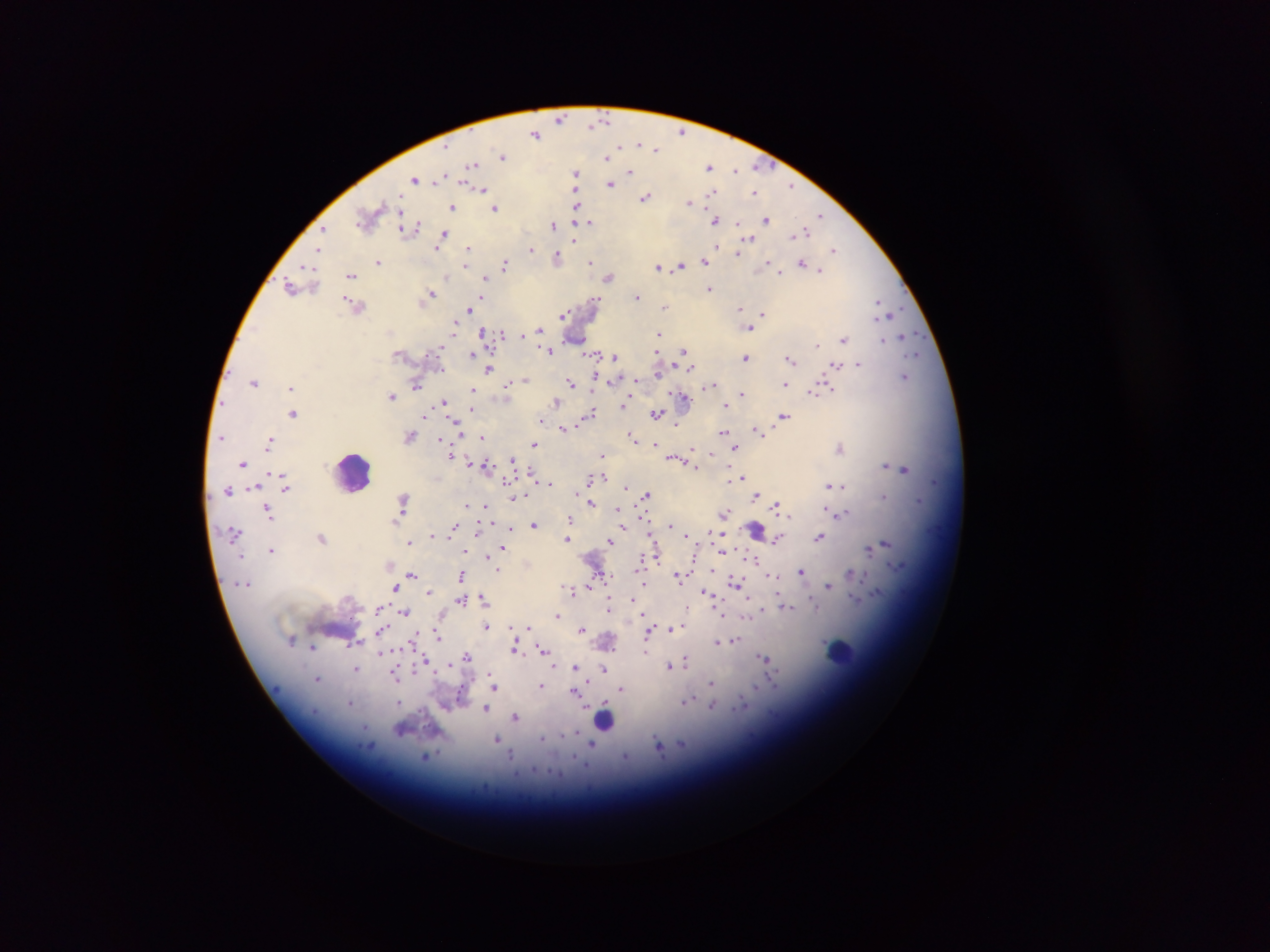

{
  "leukocyte_locations": "approximate centers as {x, y} in pixels: {353, 472}, {841, 651}, {605, 716}",
  "image_size": "1270×952 pixels",
  "field_of_view": "single",
  "country": "Ghana",
  "capture": "mobile-phone photograph through a microscope",
  "preparation": "thick blood smear",
  "plasmodium_parasite_locations": "approximate centers as {x, y} in pixels: {560, 118}, {602, 120}, {595, 122}, {682, 132}, {536, 133}, {638, 144}, {658, 147}, {503, 156}, {609, 156}, {473, 164}, {758, 166}, {710, 167}, {735, 170}, {576, 172}, {630, 172}, {441, 177}, {415, 178}, {612, 184}, {790, 188}, {482, 189}, {714, 192}, {755, 192}, {646, 196}, {576, 202}, {689, 203}, {453, 207}, {495, 208}, {369, 216}, {820, 216}, {767, 218}, {716, 219}, {589, 222}, {554, 225}, {324, 228}, {409, 228}, {801, 232}, {445, 234}, {575, 239}, {749, 239}, {441, 243}, {440, 248}, {319, 250}, {468, 250}, {530, 250}, {833, 250}, {738, 253}, {557, 257}, {705, 261}, {379, 262}, {591, 262}, {504, 264}, {768, 264}, {804, 264}, {466, 266}, {308, 267}, {659, 267}, {680, 267}, {821, 269}, {780, 272}, {350, 274}, {446, 275}, {610, 277}, {486, 279}, {291, 287}, {709, 288}, {430, 294}, {637, 295}, {596, 299}, {480, 302}, {472, 303}, {879, 303}, {354, 304}, {664, 307}, {739, 308}, {883, 308}, {469, 310}, {890, 312}, {763, 313}, {563, 315}, {454, 327}, {749, 328}, {539, 329}, {483, 332}, {504, 332}, {659, 333}, {905, 337}, {844, 339}, {884, 339}, {817, 345}, {439, 347}, {550, 349}, {684, 351}, {472, 353}, {657, 353}, {917, 353}, {597, 354}, {615, 357}, {746, 357}, {791, 359}, {858, 363}, {836, 364}, {490, 368}, {691, 368}, {905, 376}, {597, 377}, {637, 379}, {525, 380}, {254, 382}, {571, 382}, {611, 382}, {416, 384}, {710, 384}, {786, 384}, {508, 385}, {292, 387}, {824, 387}, {473, 390}, {817, 390}, {743, 393}, {393, 396}, {684, 397}, {443, 402}, {557, 402}, {624, 406}, {726, 406}, {472, 410}, {294, 412}, {591, 413}, {657, 413}, {426, 414}, {783, 416}, {541, 419}, {678, 423}, {457, 426}, {564, 427}, {757, 429}, {724, 431}, {411, 435}, {222, 437}, {482, 437}, {634, 437}, {442, 438}, {271, 441}, {535, 443}, {656, 443}, {736, 447}, {841, 447}, {693, 450}, {452, 455}, {603, 455}, {512, 458}, {675, 458}, {468, 462}, {244, 463}, {690, 463}, {474, 464}, {885, 465}, {488, 468}, {904, 469}, {531, 471}, {272, 472}, {283, 473}, {730, 477}, {741, 477}, {591, 480}, {507, 481}, {550, 483}, {624, 486}, {829, 486}, {843, 486}, {286, 487}, {256, 488}, {228, 490}, {524, 493}, {646, 495}, {757, 495}, {884, 495}, {518, 497}, {403, 501}, {919, 501}, {590, 503}, {466, 504}, {776, 504}, {487, 505}, {828, 507}, {269, 508}, {616, 510}, {725, 513}, {841, 514}, {789, 517}, {570, 519}, {535, 525}, {670, 525}, {454, 528}, {510, 528}, {624, 528}, {756, 529}, {714, 533}, {434, 534}, {687, 534}, {322, 537}, {820, 537}, {568, 538}, {777, 538}, {610, 541}, {409, 542}, {886, 543}, {503, 547}, {272, 549}, {465, 550}, {728, 550}, {869, 550}, {723, 551}, {464, 556}, {657, 557}, {756, 558}, {640, 561}, {490, 562}, {498, 569}, {801, 571}, {851, 573}, {411, 574}, {462, 575}, {602, 575}, {679, 575}, {772, 575}, {643, 583}, {736, 583}, {830, 585}, {395, 588}, {574, 589}, {429, 591}, {711, 596}, {855, 598}, {461, 599}, {483, 599}, {632, 599}, {812, 603}, {381, 606}, {608, 606}, {687, 606}, {786, 606}, {405, 611}, {558, 614}, {442, 615}, {644, 615}, {723, 615}, {749, 615}, {486, 626}, {528, 626}, {683, 626}, {670, 628}, {382, 629}, {582, 629}, {437, 633}, {647, 634}, {734, 640}, {717, 641}, {359, 642}, {413, 643}, {313, 646}, {516, 647}, {542, 650}, {646, 651}, {381, 653}, {467, 657}, {765, 658}, {426, 659}, {686, 660}, {449, 663}, {670, 666}, {576, 667}, {605, 668}, {357, 669}, {489, 671}, {396, 675}, {318, 678}, {711, 683}, {541, 685}, {495, 686}, {621, 688}, {576, 691}, {400, 701}, {686, 701}, {352, 703}, {713, 705}, {485, 709}, {516, 716}, {402, 729}, {578, 732}, {498, 740}, {593, 745}, {659, 747}, {512, 754}, {429, 756}, {625, 757}"
}